Name the parasite shown.
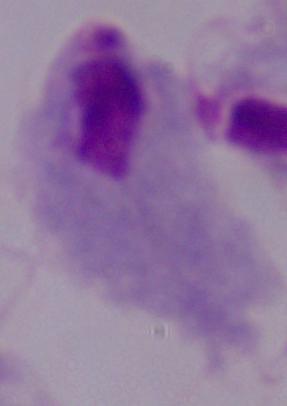
A trichomonad.

Micrograph. Captured at 1000x magnification.